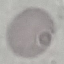

Result: no malaria parasites detected. Photographed with a smartphone camera at the microscope eyepiece. Thin blood film. Giemsa stain. Cell patch, automatically extracted from a larger field of view and resized to 64 × 64 pixels.